Assess this cell for malaria.
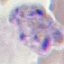
It is parasitized.

Summary:
  - Stain: Giemsa
  - Preparation: thin blood film
  - Capture: smartphone through the microscope eyepiece
  - Image type: automatically extracted cell patch, resized to 64 × 64 pixels